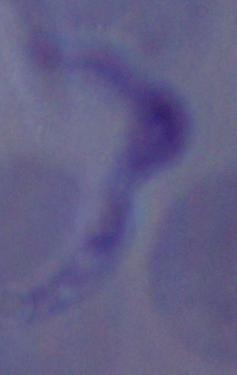
Micrograph. Captured at 1000x magnification. A trypanosome is shown.